Classify this cell by malaria status.
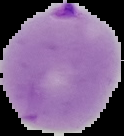
It is parasitized.

Summary:
  - Preparation: thin blood smear
  - Image type: segmented cell region on a black background
  - Image size: 124×136 pixels